Classify this cell by malaria status.
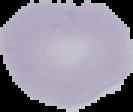
Uninfected.

image_size: 133×112 pixels
preparation: thin blood film
image_type: segmented cell region with the area outside set to black